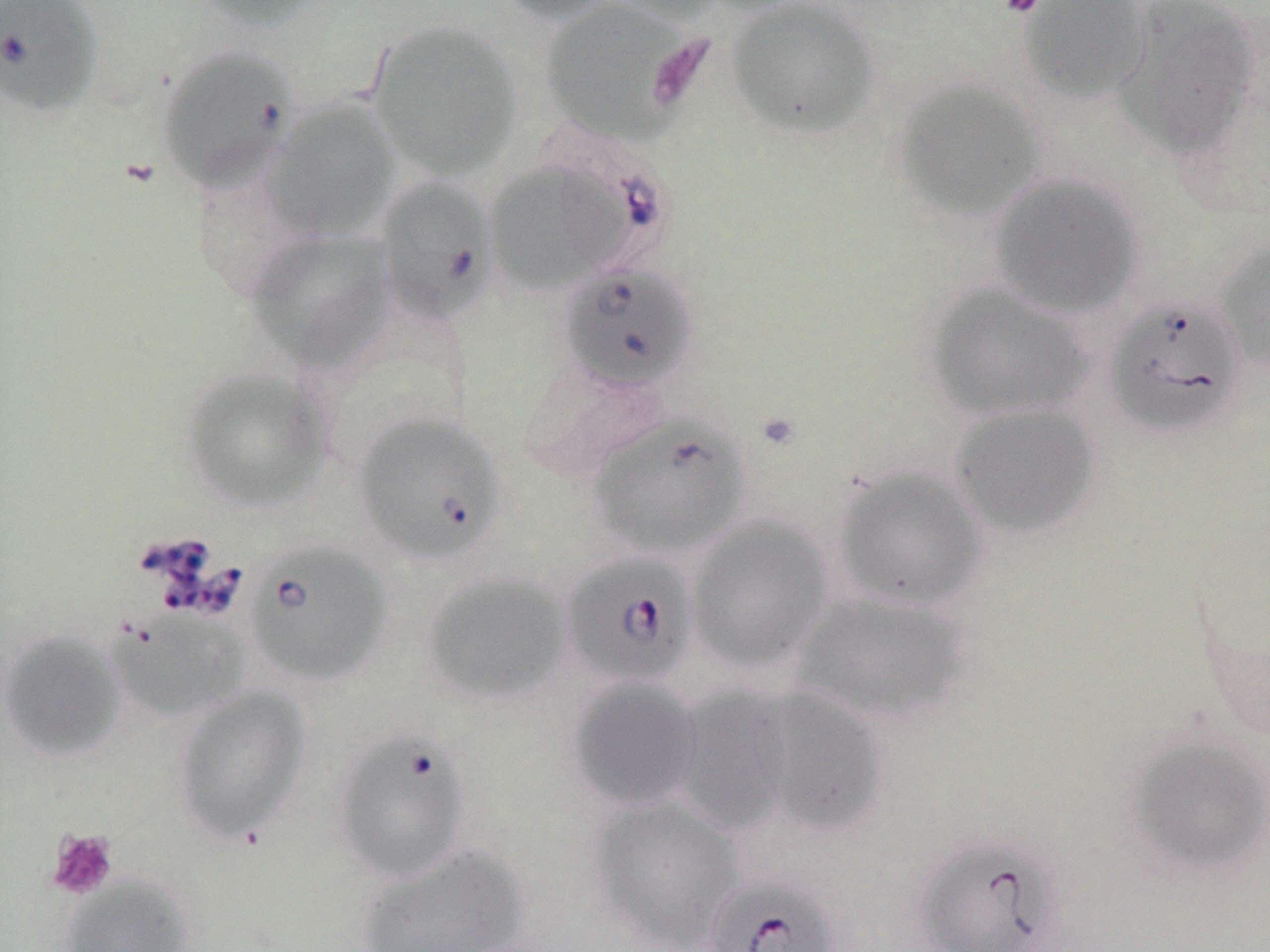
slide-level diagnosis = Babesia divergens
stain = May-Grünwald-Giemsa
field of view = one of a larger specimen
uninfected red blood cell locations = approximate bounding boxes as (x1,y1)-(x2,y2) corner pairs in pixels: (190,0)-(327,33), (491,0)-(627,24), (538,0)-(702,145), (609,0)-(728,24), (726,0)-(881,139), (1019,0)-(1153,104), (1115,0)-(1264,159), (366,18)-(524,182), (155,45)-(300,193), (893,78)-(1050,221), (263,98)-(402,240), (486,161)-(623,295), (988,173)-(1145,319), (375,177)-(499,324), (244,230)-(393,370), (1214,237)-(1270,373), (924,282)-(1094,423), (520,357)-(670,481), (179,367)-(333,512), (948,402)-(1101,540), (833,465)-(990,612), (687,515)-(834,675), (421,570)-(573,707), (790,591)-(973,728), (105,611)-(250,725), (1,629)-(127,763), (566,676)-(704,813), (727,683)-(892,842), (170,685)-(312,845), (1125,731)-(1270,879), (586,796)-(745,950), (354,843)-(529,952), (58,875)-(196,952)
magnification = 1000x
platelet locations = approximate bounding boxes as (x1,y1)-(x2,y2) corner pairs in pixels: (997,0)-(1046,18), (46,828)-(119,900)
Babesia divergens-infected red blood cell locations = approximate bounding boxes as (x1,y1)-(x2,y2) corner pairs in pixels: (0,0)-(107,120), (559,263)-(698,392), (1105,297)-(1246,438), (354,411)-(506,564), (588,413)-(752,561), (244,540)-(393,687), (560,552)-(700,689), (330,726)-(474,885), (910,831)-(1075,952), (702,873)-(843,952)
preparation = thin blood film
modality = light microscopy
image size = 1270×952 pixels